Report the malaria status.
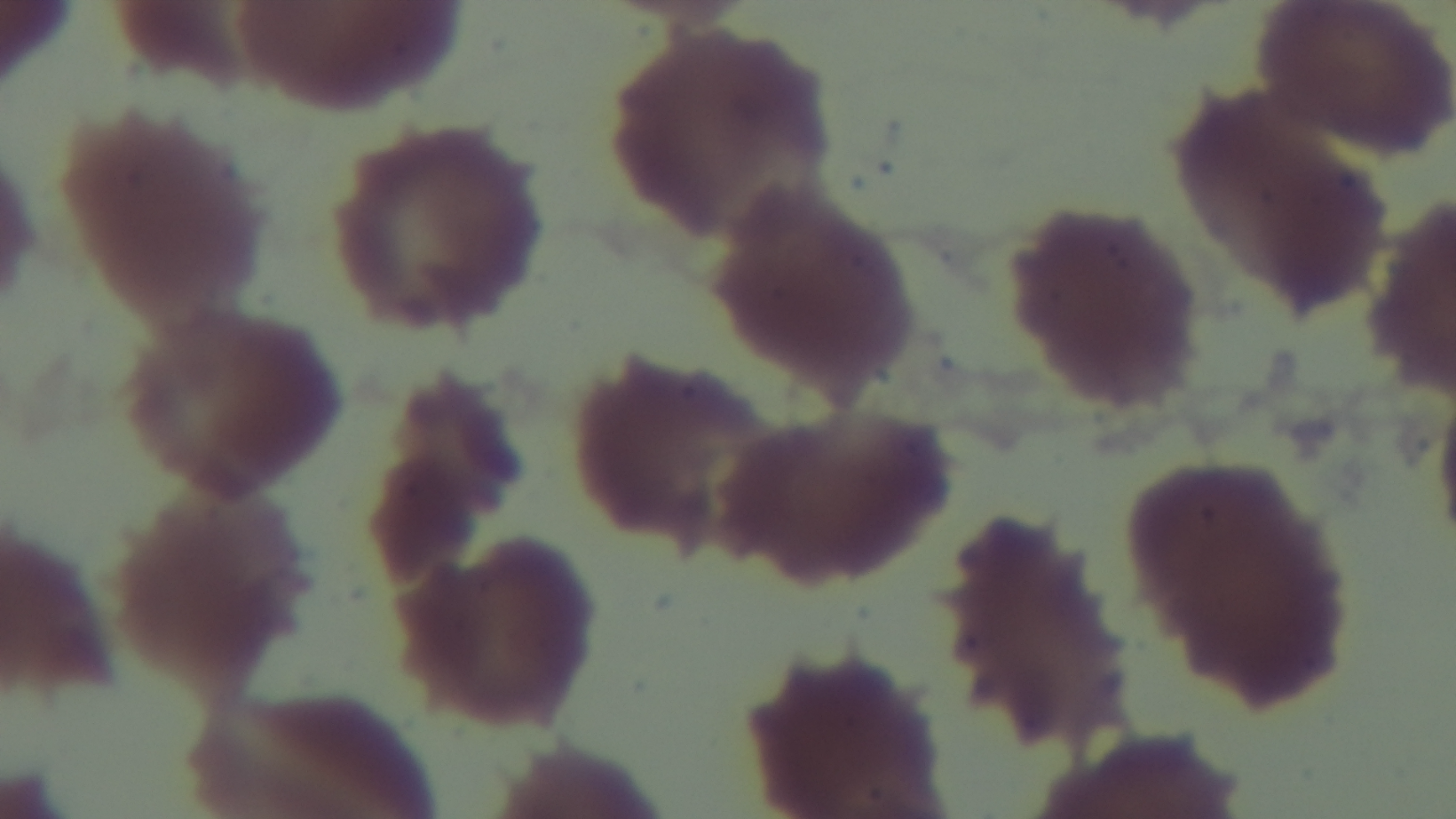
It is uninfected.

Giemsa-stained. Oil-immersion objective, 100x. Captured with a mounted 4K digital camera. One field from the slide. Photomicrograph. Preparation: thin blood film.